State the blood parasite species.
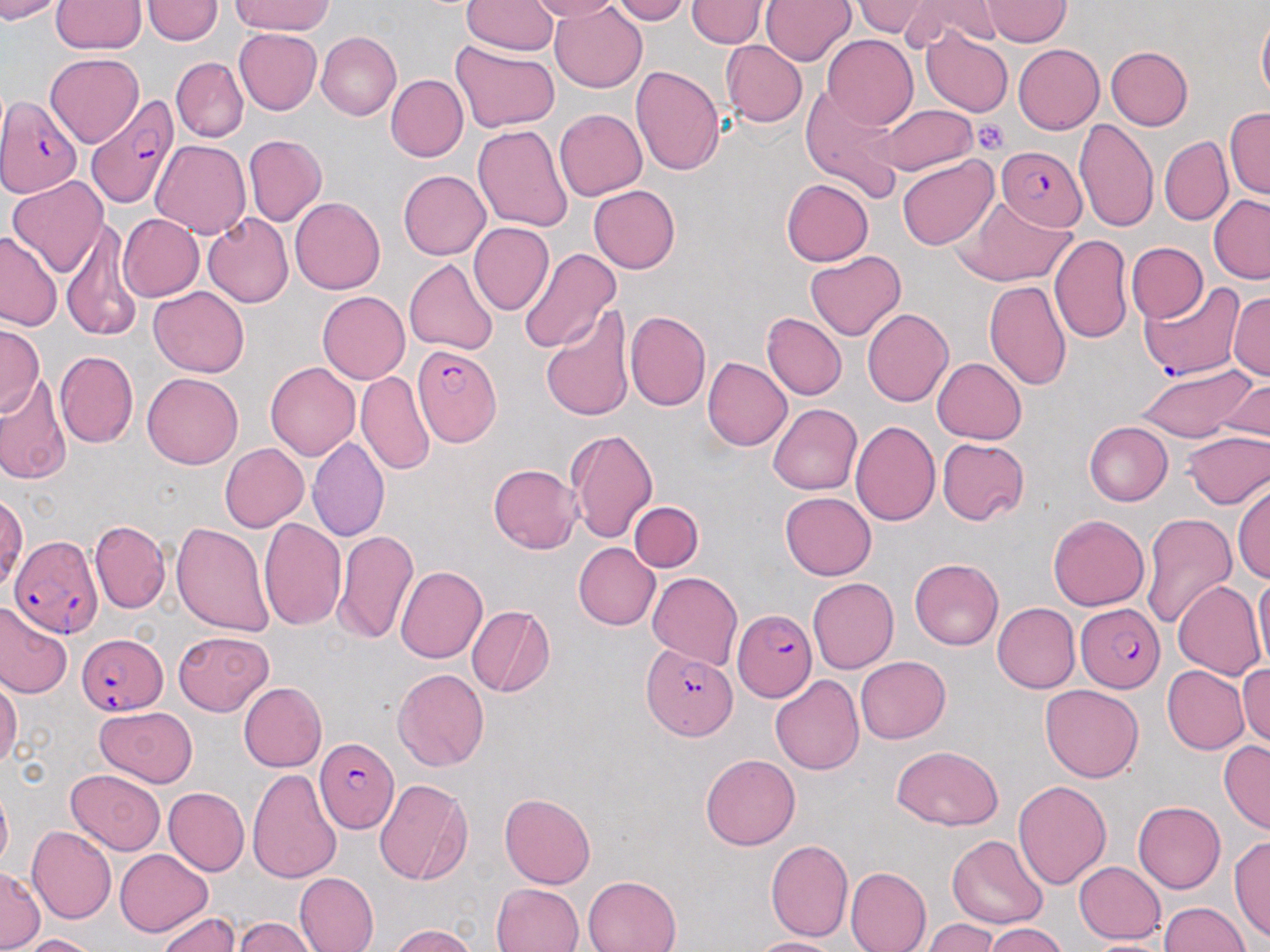

Plasmodium falciparum.

Approximate bounding boxes as named x1/y1/x2/y2 corners in pixels. Uninfected red blood cell locations: (x1=0, y1=0, x2=66, y2=23), (x1=233, y1=0, x2=333, y2=35), (x1=611, y1=0, x2=691, y2=24), (x1=686, y1=0, x2=772, y2=49), (x1=760, y1=0, x2=856, y2=65), (x1=904, y1=0, x2=1005, y2=51), (x1=51, y1=1, x2=147, y2=53), (x1=142, y1=1, x2=223, y2=44), (x1=461, y1=1, x2=559, y2=55), (x1=528, y1=1, x2=624, y2=22), (x1=853, y1=1, x2=937, y2=41), (x1=980, y1=1, x2=1072, y2=46), (x1=550, y1=3, x2=647, y2=93), (x1=1257, y1=12, x2=1270, y2=105), (x1=233, y1=28, x2=322, y2=114), (x1=920, y1=30, x2=1012, y2=116), (x1=316, y1=32, x2=401, y2=121), (x1=822, y1=35, x2=918, y2=129), (x1=449, y1=40, x2=559, y2=134), (x1=721, y1=41, x2=808, y2=127), (x1=1013, y1=44, x2=1104, y2=134), (x1=1105, y1=46, x2=1193, y2=130), (x1=45, y1=52, x2=143, y2=147), (x1=171, y1=57, x2=249, y2=142), (x1=630, y1=64, x2=725, y2=176), (x1=386, y1=74, x2=467, y2=162), (x1=800, y1=85, x2=908, y2=201), (x1=877, y1=102, x2=977, y2=176), (x1=1225, y1=106, x2=1270, y2=200), (x1=553, y1=108, x2=647, y2=201), (x1=1074, y1=119, x2=1158, y2=234), (x1=472, y1=125, x2=574, y2=233), (x1=243, y1=134, x2=326, y2=226), (x1=1160, y1=136, x2=1233, y2=226), (x1=150, y1=140, x2=251, y2=238), (x1=896, y1=154, x2=998, y2=250), (x1=398, y1=171, x2=491, y2=260), (x1=7, y1=177, x2=109, y2=277), (x1=782, y1=178, x2=873, y2=266), (x1=589, y1=185, x2=680, y2=274), (x1=1209, y1=196, x2=1270, y2=284), (x1=956, y1=197, x2=1074, y2=287), (x1=289, y1=198, x2=385, y2=294), (x1=118, y1=213, x2=203, y2=302), (x1=203, y1=213, x2=294, y2=308), (x1=60, y1=217, x2=143, y2=341), (x1=468, y1=221, x2=553, y2=315), (x1=0, y1=231, x2=62, y2=329), (x1=1049, y1=234, x2=1133, y2=344), (x1=1126, y1=242, x2=1208, y2=322), (x1=518, y1=248, x2=621, y2=354), (x1=804, y1=251, x2=905, y2=341), (x1=405, y1=258, x2=499, y2=356), (x1=1003, y1=260, x2=1121, y2=372), (x1=984, y1=281, x2=1072, y2=392), (x1=148, y1=286, x2=249, y2=376), (x1=317, y1=291, x2=410, y2=383), (x1=1228, y1=293, x2=1270, y2=381), (x1=540, y1=305, x2=634, y2=422), (x1=862, y1=308, x2=954, y2=407), (x1=623, y1=310, x2=711, y2=410), (x1=762, y1=312, x2=846, y2=399), (x1=0, y1=322, x2=44, y2=414), (x1=54, y1=351, x2=138, y2=448), (x1=702, y1=357, x2=793, y2=450), (x1=933, y1=358, x2=1027, y2=444), (x1=265, y1=361, x2=360, y2=461), (x1=1131, y1=363, x2=1257, y2=444), (x1=142, y1=372, x2=243, y2=469), (x1=355, y1=372, x2=434, y2=475), (x1=0, y1=373, x2=72, y2=485), (x1=1219, y1=377, x2=1269, y2=441), (x1=769, y1=403, x2=862, y2=496), (x1=851, y1=420, x2=940, y2=525), (x1=1084, y1=422, x2=1173, y2=506), (x1=565, y1=428, x2=658, y2=543), (x1=1181, y1=431, x2=1270, y2=510), (x1=307, y1=435, x2=390, y2=542), (x1=936, y1=438, x2=1029, y2=526), (x1=219, y1=443, x2=309, y2=533), (x1=488, y1=463, x2=582, y2=553), (x1=1232, y1=481, x2=1270, y2=582), (x1=780, y1=492, x2=876, y2=579), (x1=1, y1=494, x2=28, y2=592), (x1=629, y1=501, x2=703, y2=572), (x1=1140, y1=513, x2=1237, y2=629), (x1=1048, y1=515, x2=1149, y2=611), (x1=259, y1=517, x2=346, y2=630), (x1=90, y1=520, x2=170, y2=613), (x1=171, y1=521, x2=273, y2=635), (x1=334, y1=528, x2=419, y2=646), (x1=573, y1=542, x2=660, y2=630), (x1=910, y1=557, x2=1003, y2=650), (x1=395, y1=566, x2=487, y2=664), (x1=647, y1=572, x2=743, y2=670), (x1=1253, y1=573, x2=1270, y2=671), (x1=807, y1=578, x2=898, y2=674), (x1=1172, y1=581, x2=1265, y2=680), (x1=0, y1=601, x2=71, y2=699), (x1=992, y1=602, x2=1080, y2=692), (x1=466, y1=605, x2=554, y2=697), (x1=173, y1=630, x2=273, y2=715), (x1=172, y1=647, x2=312, y2=762), (x1=856, y1=656, x2=950, y2=743), (x1=1237, y1=662, x2=1269, y2=750), (x1=1162, y1=665, x2=1250, y2=755), (x1=392, y1=668, x2=489, y2=770), (x1=0, y1=675, x2=22, y2=772), (x1=770, y1=675, x2=864, y2=775), (x1=238, y1=682, x2=327, y2=771), (x1=1040, y1=683, x2=1144, y2=783), (x1=95, y1=706, x2=197, y2=788), (x1=1219, y1=739, x2=1270, y2=834), (x1=890, y1=745, x2=1003, y2=831), (x1=700, y1=754, x2=800, y2=850), (x1=65, y1=769, x2=165, y2=855), (x1=247, y1=769, x2=343, y2=884), (x1=373, y1=778, x2=473, y2=886), (x1=1013, y1=780, x2=1112, y2=889), (x1=0, y1=785, x2=11, y2=871), (x1=163, y1=787, x2=250, y2=875), (x1=499, y1=792, x2=595, y2=889), (x1=1132, y1=801, x2=1225, y2=893), (x1=26, y1=826, x2=116, y2=925), (x1=1229, y1=834, x2=1270, y2=943), (x1=946, y1=835, x2=1047, y2=929), (x1=766, y1=839, x2=853, y2=941), (x1=114, y1=848, x2=212, y2=937), (x1=1073, y1=861, x2=1166, y2=943), (x1=846, y1=866, x2=932, y2=952), (x1=0, y1=867, x2=42, y2=951), (x1=294, y1=872, x2=379, y2=952), (x1=582, y1=875, x2=681, y2=952), (x1=491, y1=882, x2=583, y2=952), (x1=1157, y1=902, x2=1251, y2=952), (x1=156, y1=911, x2=239, y2=952), (x1=232, y1=917, x2=320, y2=952), (x1=922, y1=919, x2=999, y2=951), (x1=984, y1=923, x2=1069, y2=952), (x1=389, y1=924, x2=478, y2=952), (x1=17, y1=934, x2=100, y2=952), (x1=747, y1=938, x2=845, y2=952), (x1=1078, y1=939, x2=1180, y2=951). Plasmodium falciparum-infected red blood cell locations: (x1=84, y1=95, x2=182, y2=210), (x1=0, y1=96, x2=81, y2=199), (x1=994, y1=147, x2=1086, y2=231), (x1=1140, y1=284, x2=1249, y2=377), (x1=410, y1=342, x2=502, y2=448), (x1=8, y1=533, x2=101, y2=636), (x1=1075, y1=601, x2=1164, y2=692), (x1=732, y1=609, x2=816, y2=701), (x1=76, y1=632, x2=169, y2=714), (x1=641, y1=643, x2=735, y2=738), (x1=314, y1=738, x2=399, y2=832). Platelet locations: (x1=970, y1=119, x2=1009, y2=155). 1000x magnification. Thin blood smear. May-Grünwald-Giemsa stain. Image is 1270×952 pixels. Single field of view. Light microscopy.